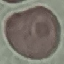

malaria status = uninfected
image type = cell patch, automatically extracted from a larger field of view and resized to 64 × 64 pixels
preparation = thin smear
capture = smartphone through the microscope eyepiece
stain = Giemsa